Assess this cell for malaria.
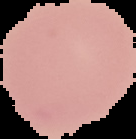
Uninfected.

Segmented cell region on a black background. From a thin blood film. Image is 136×139 pixels.